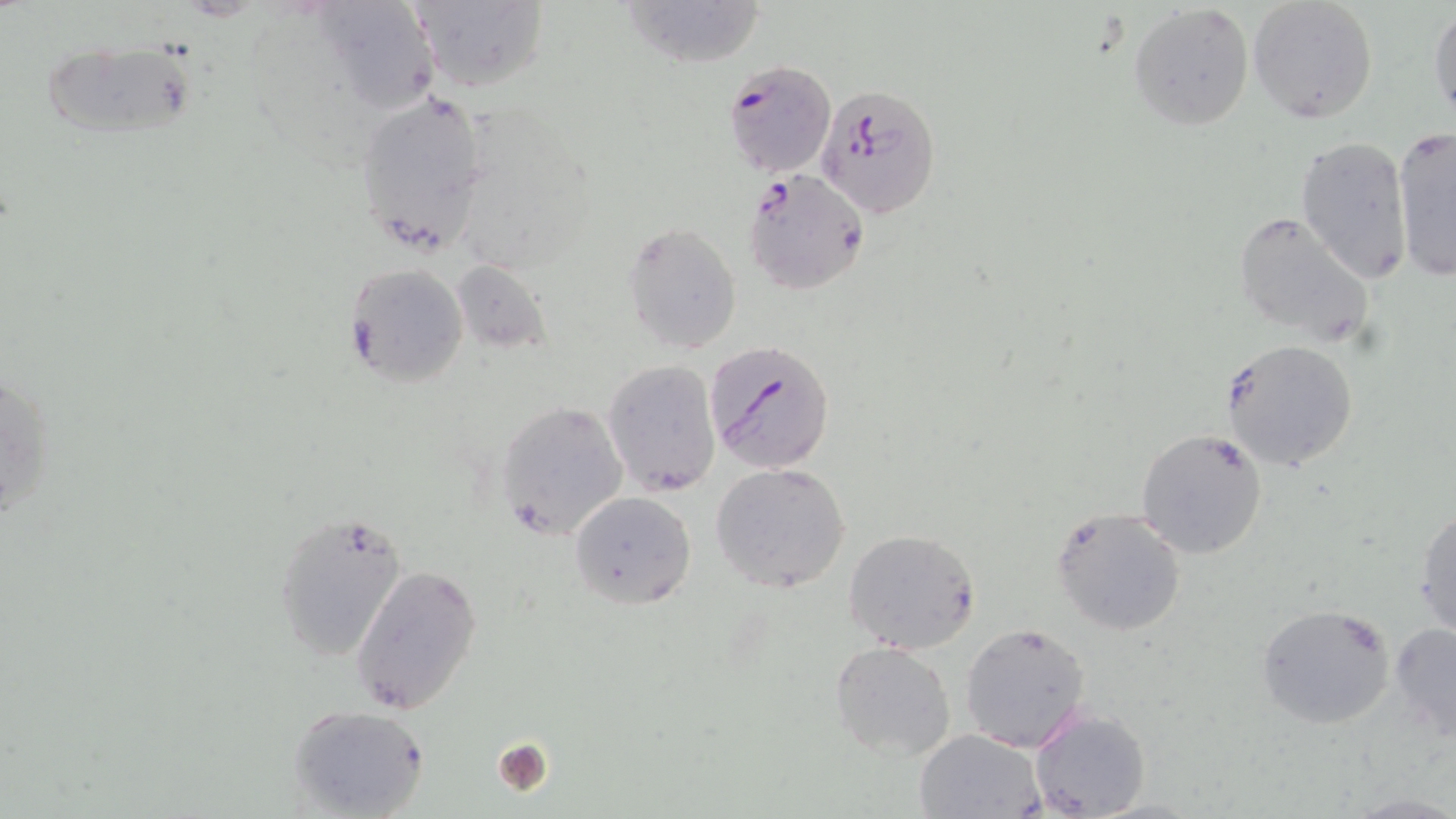
Approximate bounding boxes as [x1, y1, x2, y2] in pixels. Plasmodium falciparum-infected red blood cell locations: [724, 59, 838, 178], [816, 85, 941, 217], [743, 170, 871, 295], [704, 340, 835, 474]. Uninfected red blood cell locations: [409, 0, 549, 93], [619, 0, 768, 68], [1247, 0, 1379, 124], [308, 1, 441, 111], [1129, 3, 1255, 132], [1428, 6, 1456, 129], [39, 38, 207, 144], [355, 86, 493, 251], [1396, 129, 1456, 280], [1295, 135, 1417, 284], [1230, 210, 1374, 347], [622, 222, 742, 354], [448, 259, 549, 354], [345, 261, 468, 386], [1221, 339, 1359, 471], [602, 360, 723, 496], [0, 363, 56, 531], [496, 400, 631, 544], [1136, 427, 1269, 560], [711, 461, 852, 593], [570, 490, 696, 608], [1413, 504, 1456, 641], [1050, 506, 1185, 637], [273, 510, 408, 661], [842, 529, 980, 655], [351, 562, 483, 715], [1256, 603, 1395, 729], [1388, 621, 1456, 741], [960, 622, 1093, 753], [829, 640, 956, 761], [287, 705, 430, 819], [1028, 708, 1151, 819], [914, 729, 1044, 818]. Platelet locations: [492, 737, 555, 797]. Slide-level diagnosis: Plasmodium falciparum. Optical microscopy. Thin blood film. Image is 1456×819 pixels. One field of a larger specimen. May-Grünwald-Giemsa stain. 1000x magnification.